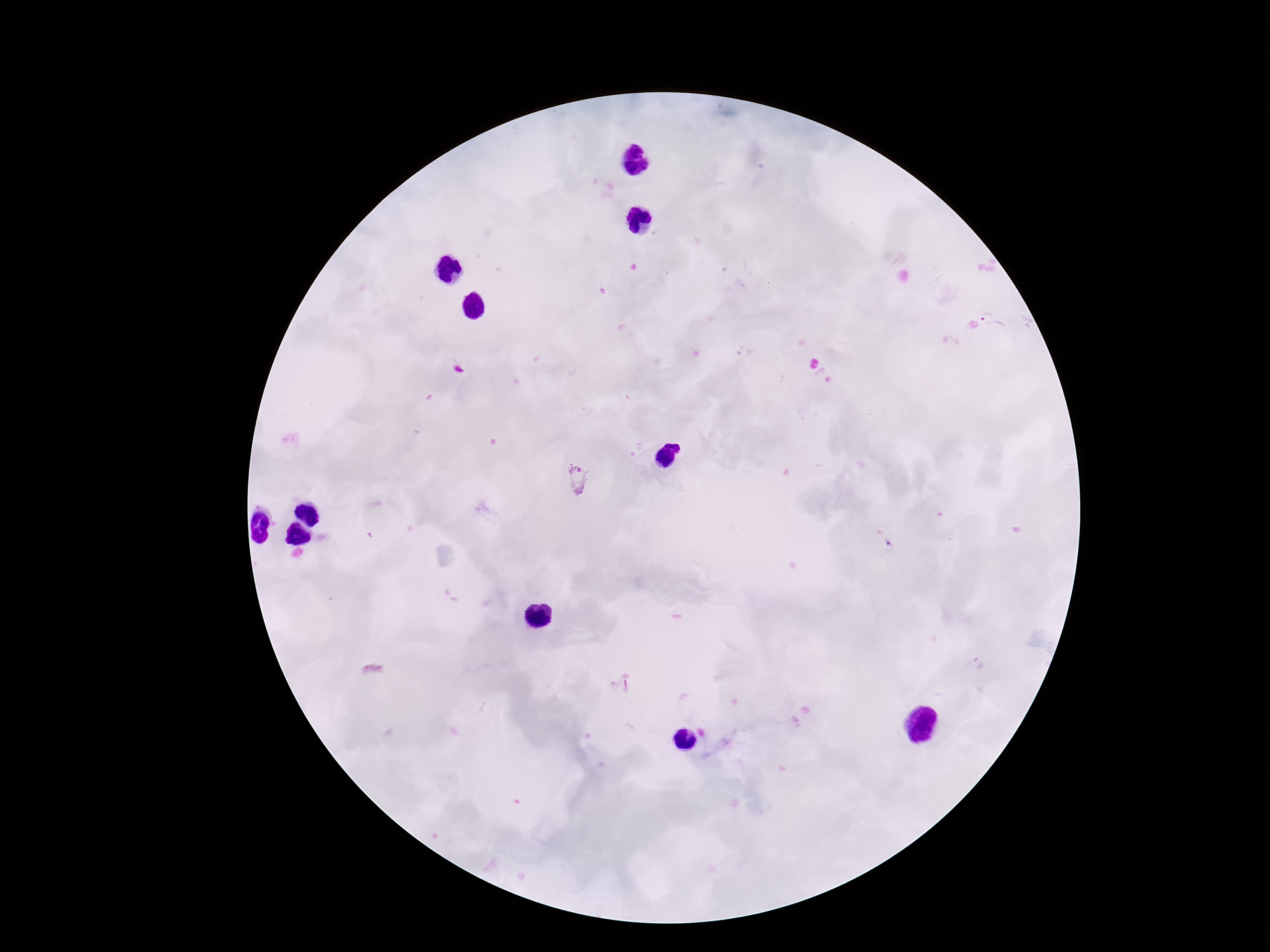

{
  "field_of_view": "one from this slide",
  "image_size": "1270×952 pixels",
  "stain": "Giemsa",
  "plasmodium_parasite_locations": "approximate centers as (x, y) in pixels: (995, 320), (576, 480), (890, 545), (976, 664), (621, 685)",
  "preparation": "thick blood smear",
  "capture": "smartphone camera through the microscope eyepiece",
  "patient_malaria_status": "infected",
  "magnification": "100x"
}